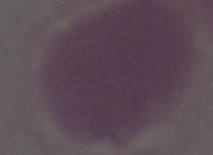

Summary:
  - Identification: erythrocyte
  - Magnification: 1000x
  - Modality: micrograph